Give the position of every malaria parasite and every leukocyte.
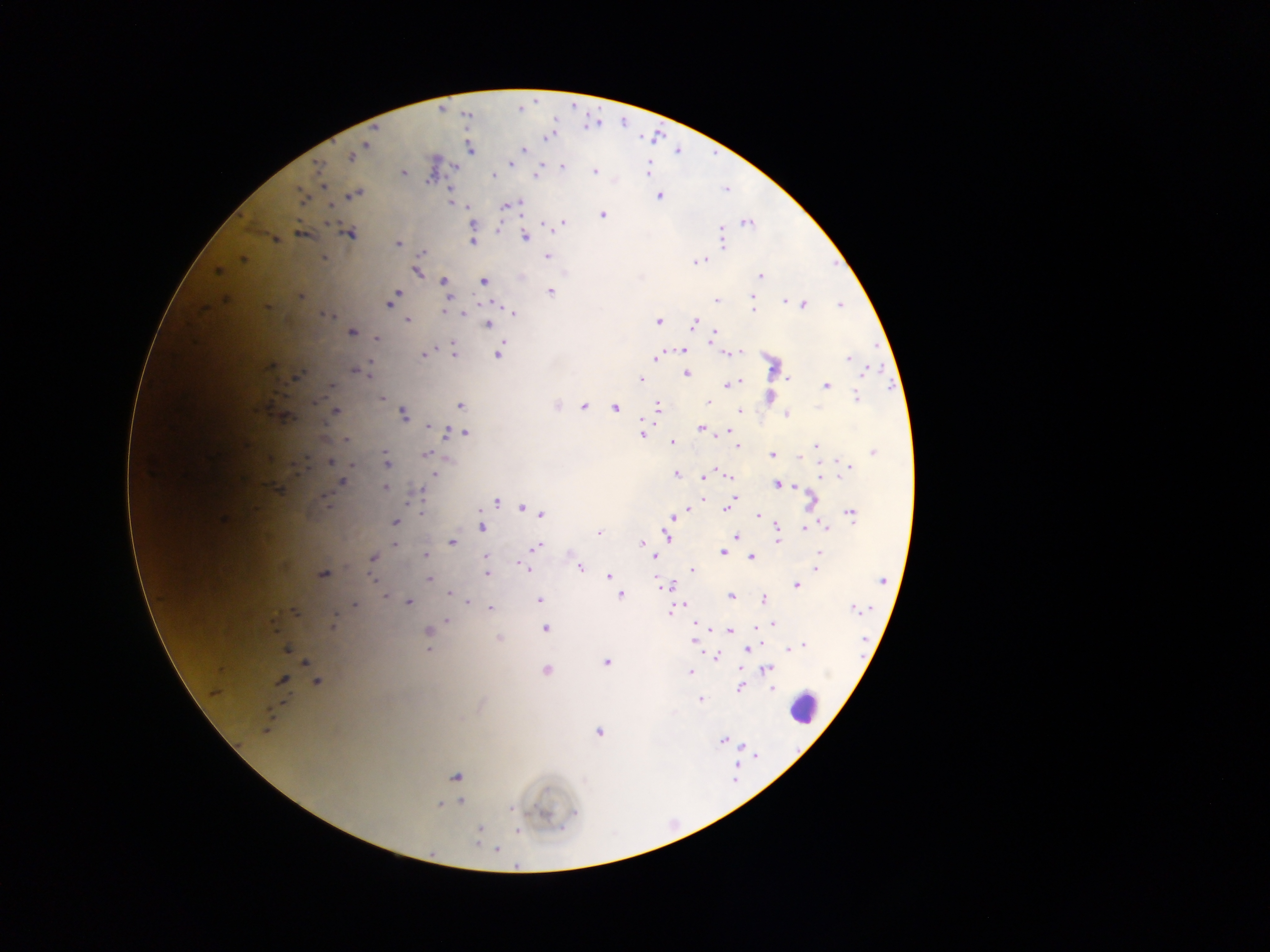
Approximate centers as x y in pixels.
Malaria parasites: 470 149; 523 149; 352 155; 511 162; 562 166; 319 170; 647 170; 403 172; 594 172; 537 174; 493 175; 355 194; 303 195; 659 195; 451 203; 510 204; 504 206; 466 208; 602 215; 329 221; 562 222; 747 223; 549 224; 721 227; 349 233; 722 233; 301 234; 525 237; 275 239; 472 241; 397 243; 723 243; 422 253; 546 256; 323 257; 242 259; 697 261; 417 271; 217 272; 761 275; 443 281; 483 281; 550 291; 394 293; 301 296; 751 296; 447 297; 716 299; 391 300; 784 301; 804 304; 839 304; 267 306; 444 311; 462 312; 512 313; 326 314; 408 320; 658 321; 487 324; 693 324; 351 331; 714 331; 711 336; 376 338; 683 350; 498 352; 741 352; 455 353; 727 353; 425 354; 657 357; 847 358; 268 366; 370 366; 354 369; 360 371; 865 371; 686 373; 295 377; 640 378; 739 380; 330 384; 727 384; 825 384; 383 398; 856 399; 708 402; 460 406; 583 406; 615 407; 657 407; 739 409; 335 411; 402 413; 788 414; 428 425; 702 428; 447 431; 726 431; 459 433; 465 433; 642 434; 345 439; 671 441; 737 447; 815 447; 873 452; 425 453; 772 455; 329 462; 349 463; 386 463; 848 466; 433 473; 676 473; 822 476; 730 477; 702 478; 342 481; 777 484; 795 486; 384 487; 277 489; 421 492; 704 497; 732 500; 495 501; 810 503; 521 508; 726 509; 687 511; 421 512; 480 512; 540 513; 850 513; 678 515; 758 515; 671 518; 223 519; 395 522; 481 526; 807 526; 824 526; 776 527; 805 529; 599 533; 666 535; 737 536; 452 541; 776 542; 393 543; 641 543; 536 546; 726 546; 723 552; 819 552; 425 554; 372 557; 486 557; 750 557; 654 558; 579 567; 815 567; 526 568; 691 570; 322 574; 487 574; 607 577; 657 577; 373 579; 429 579; 882 580; 796 584; 669 587; 449 592; 620 594; 385 596; 731 596; 764 599; 408 600; 539 600; 466 601; 354 605; 686 605; 490 607; 853 607; 293 612; 669 612; 447 621; 773 623; 332 626; 544 628; 755 629; 729 630; 427 631; 498 639; 694 641; 804 646; 788 647; 286 648; 428 649; 747 649; 715 656; 606 662; 304 663; 741 668; 766 669; 546 670; 691 672; 280 680; 317 681; 741 686; 772 687; 701 700; 599 732; 723 740; 455 776; 460 800; 440 803; 479 829; 518 830; 496 849.
Leukocytes: 805 708.

field_of_view: single
image_size: 1270×952 pixels
capture: mobile-phone photograph through a microscope
country: Ghana
preparation: thick blood film